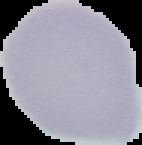

malaria status = uninfected
preparation = thin blood smear
image type = segmented cell region on a black background
image size = 142×145 pixels